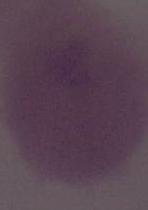

Summary:
  - Magnification: 1000x
  - Modality: photomicrograph
  - Identification: red blood cell